Locate every blood parasite and identify its species.
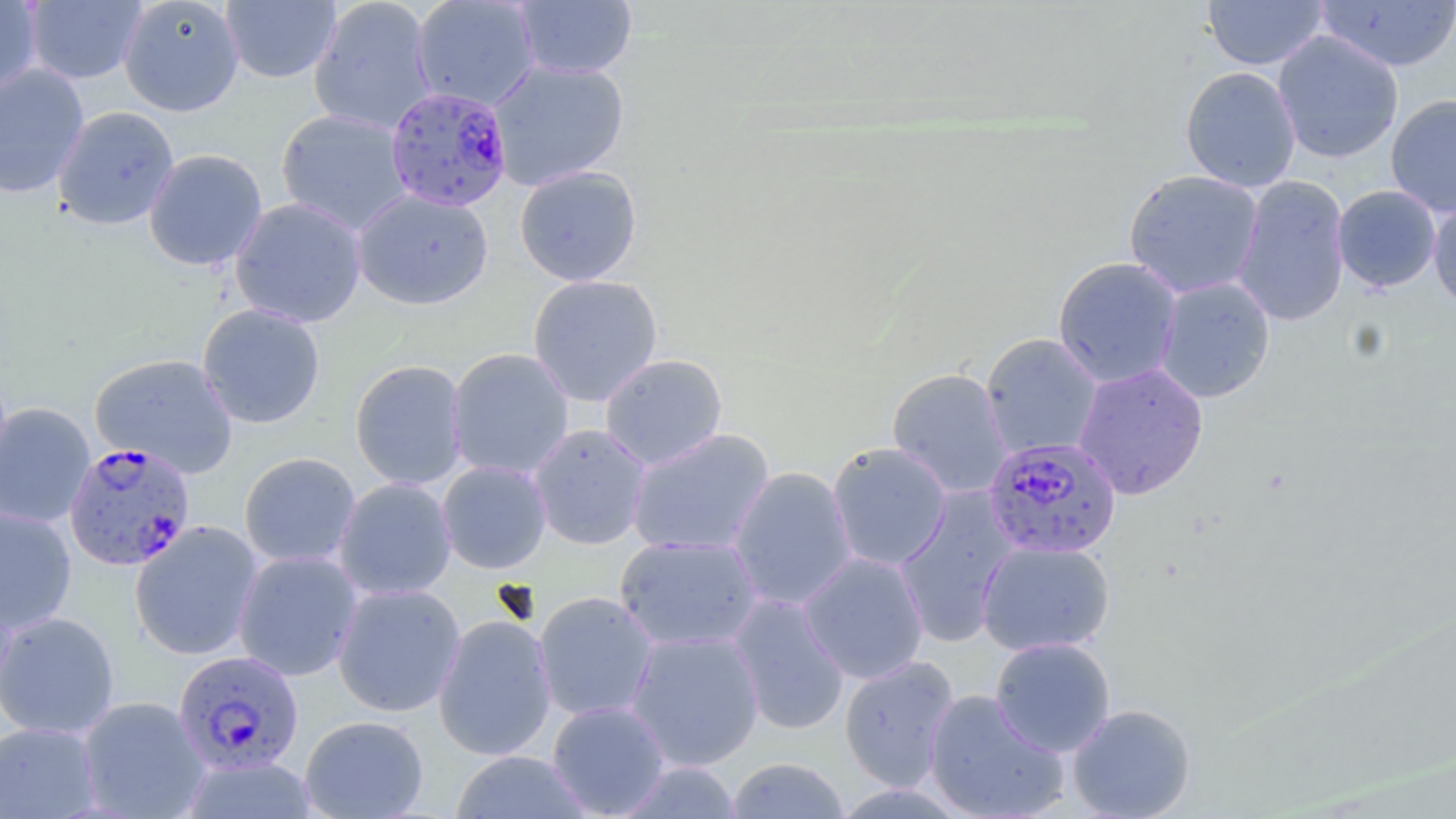
Approximate bounding boxes as (x1,y1)-(x2,y2) corner pairs in pixels.
Plasmodium falciparum-infected red blood cells: (386,86)-(513,212), (984,437)-(1122,559), (63,441)-(196,571), (172,650)-(305,776).
No Plasmodium ovale, Plasmodium malariae, Plasmodium vivax, Babesia divergens, or Trypanosoma brucei observed.

Uninfected red blood cell locations: (0,0)-(42,95), (23,0)-(147,85), (118,0)-(244,117), (308,0)-(437,136), (411,0)-(540,111), (514,0)-(637,80), (1203,0)-(1329,70), (221,1)-(341,84), (1315,1)-(1456,73), (1272,29)-(1404,164), (487,59)-(630,191), (0,64)-(90,199), (1179,66)-(1301,192), (1386,94)-(1456,218), (52,105)-(180,231), (275,108)-(413,235), (143,149)-(268,271), (514,165)-(642,287), (1123,170)-(1264,298), (1232,174)-(1350,327), (1332,185)-(1442,292), (352,189)-(494,310), (229,196)-(367,328), (1428,198)-(1456,312), (1052,256)-(1183,388), (527,274)-(664,406), (1154,277)-(1275,403), (197,303)-(326,429), (981,333)-(1104,460), (446,348)-(574,480), (89,352)-(238,478), (599,353)-(728,470), (349,358)-(469,490), (1073,362)-(1209,500), (887,367)-(1013,499), (0,402)-(95,529), (528,423)-(652,550), (626,428)-(775,557), (827,442)-(952,572), (239,452)-(361,569), (437,459)-(552,574), (727,466)-(858,612), (333,477)-(457,601), (894,487)-(1020,647), (0,506)-(77,633), (129,520)-(264,661), (614,535)-(763,652), (976,539)-(1115,657), (232,550)-(363,681), (798,552)-(930,684), (332,583)-(466,717), (533,591)-(659,722), (726,594)-(851,736), (0,611)-(120,740), (432,613)-(558,761), (624,629)-(765,771), (989,637)-(1116,757), (838,655)-(960,792), (923,689)-(1070,819), (76,696)-(211,819), (547,700)-(670,818), (1067,703)-(1196,819), (299,715)-(429,819), (0,721)-(101,819), (450,750)-(595,818), (181,756)-(318,819), (725,757)-(850,818), (617,760)-(741,817). Slide-level diagnosis: Plasmodium falciparum. Image is 1456×819 pixels. May-Grünwald-Giemsa-stained preparation. 1000x magnification. Thin blood film. Optical microscopy. One field of a larger specimen.